Give the position of every malaria parasite.
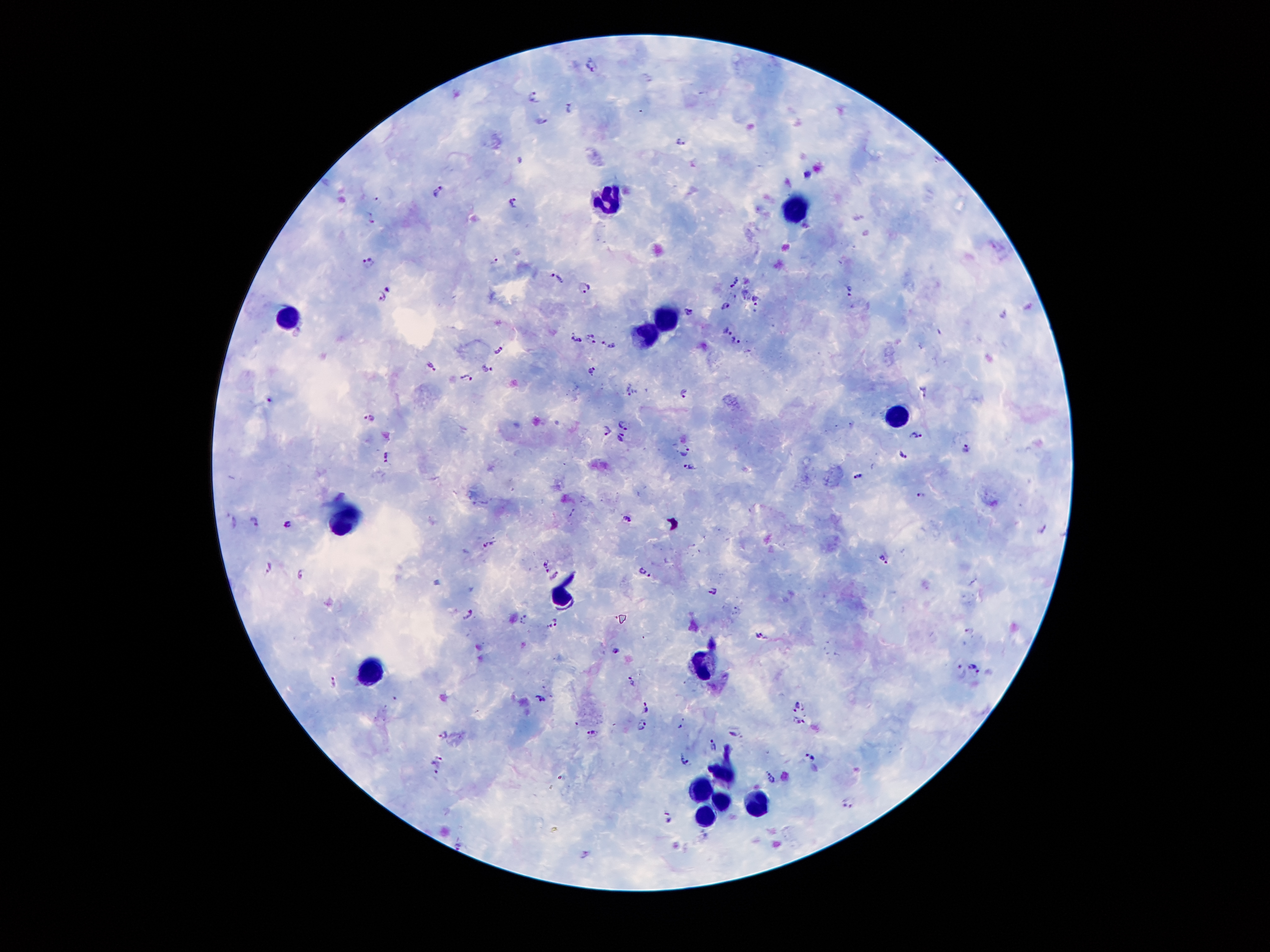

Approximate centers as [x, y] in pixels.
Malaria parasites: [591, 65], [533, 98], [572, 111], [680, 142], [438, 192], [514, 202], [371, 217], [493, 259], [367, 261], [558, 279], [732, 281], [390, 287], [583, 287], [847, 289], [744, 293], [381, 296], [758, 302], [726, 305], [690, 312], [727, 331], [590, 333], [577, 340], [736, 341], [593, 342], [607, 344], [498, 350], [432, 368], [484, 369], [592, 369], [467, 376], [631, 391], [684, 391], [925, 393], [269, 400], [372, 419], [624, 425], [608, 429], [917, 435], [621, 437], [968, 448], [685, 450], [903, 455], [385, 456], [689, 465], [859, 476], [920, 494], [255, 520], [625, 520], [235, 522], [289, 524], [489, 544], [884, 560], [547, 564], [268, 567], [645, 573], [301, 575], [553, 576], [713, 589], [469, 614], [524, 619], [553, 623], [758, 635], [616, 651], [977, 669], [958, 673], [633, 680], [335, 682], [394, 698], [541, 698], [645, 707], [799, 707], [798, 723], [643, 725], [594, 732], [442, 735], [737, 738], [713, 745], [440, 757], [684, 758], [810, 758], [435, 769], [770, 777], [849, 803], [670, 818], [458, 845], [585, 854].

Leukocyte locations: [612, 199], [796, 216], [287, 319], [665, 323], [647, 329], [894, 416], [340, 524], [561, 597], [697, 663], [375, 668], [727, 770], [699, 792], [719, 799], [758, 802], [706, 814]. Image is 1270×952 pixels. Photographed through the microscope eyepiece with a smartphone camera. 100x magnification. Thick peripheral-blood smear. One field from this slide. Giemsa-stained preparation. Patient malaria status: infected with Plasmodium falciparum.